Evaluate for Plasmodium parasites.
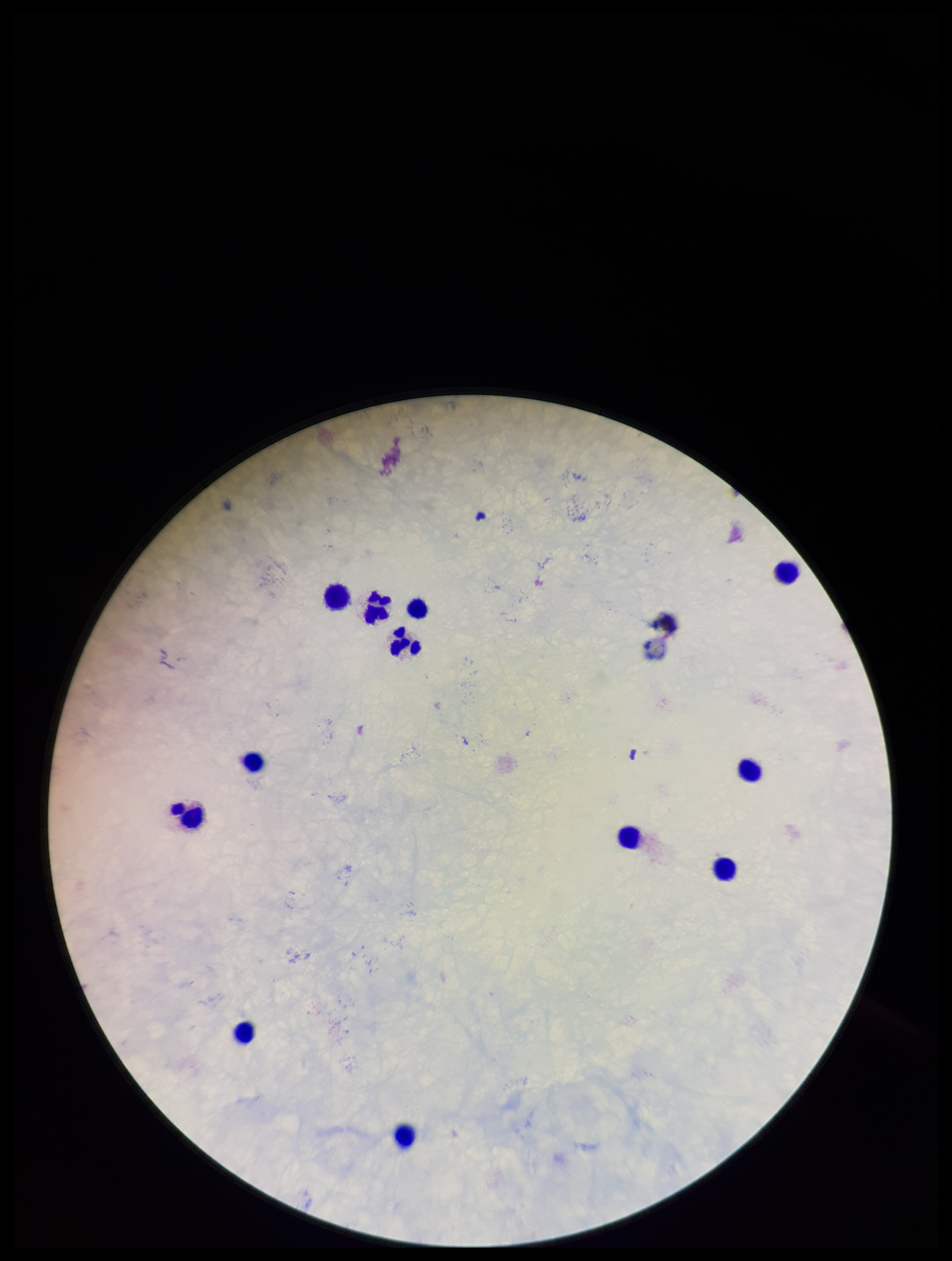
None seen.

stain = Giemsa
field of view = one from this slide
capture = smartphone photograph through the microscope eyepiece
leukocyte count = 12
patient malaria status = negative
image size = 952×1261 pixels
parasite count = 0
preparation = thick smear